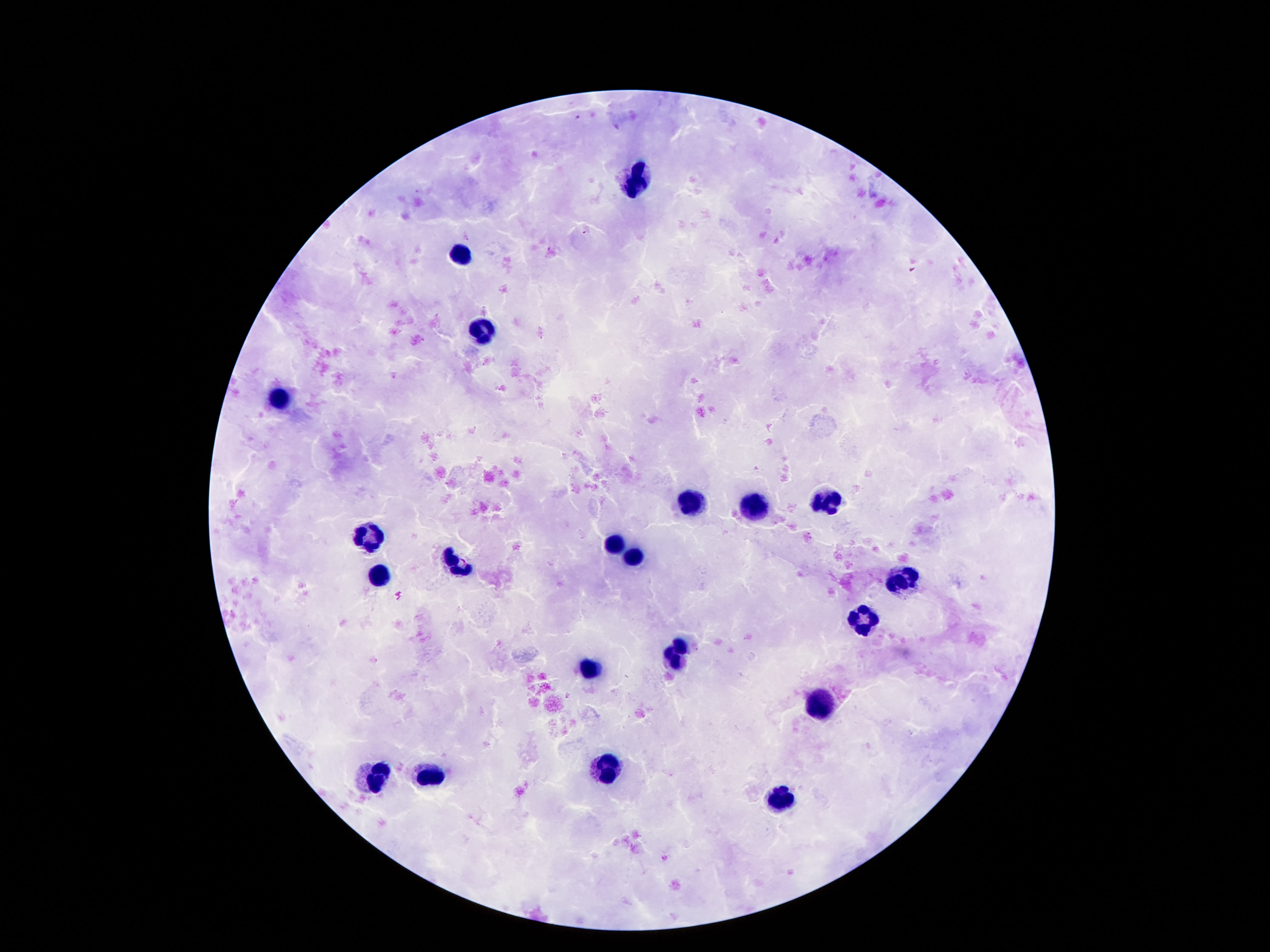

{
  "preparation": "thick blood smear",
  "stain": "Giemsa",
  "leukocyte_locations": "approximate object centers, in pixels from the top-left corner: (x=636, y=180), (x=463, y=254), (x=482, y=332), (x=281, y=395), (x=690, y=502), (x=827, y=502), (x=753, y=511), (x=369, y=539), (x=612, y=546), (x=633, y=558), (x=455, y=563), (x=377, y=574), (x=900, y=579), (x=862, y=622), (x=680, y=649), (x=587, y=669), (x=820, y=705), (x=608, y=770), (x=430, y=772), (x=371, y=781), (x=778, y=799)",
  "field_of_view": "one from this slide",
  "magnification": "100x",
  "image_size": "1270×952 pixels",
  "patient_malaria_status": "negative",
  "capture": "smartphone camera through the microscope eyepiece"
}